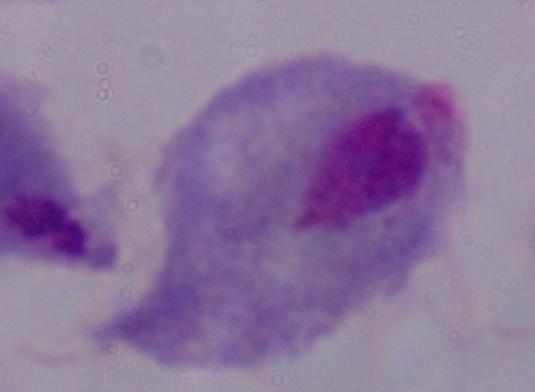
Summary:
  - Identification: trichomonad
  - Magnification: 1000x
  - Modality: photomicrograph